Identify the blood parasite species.
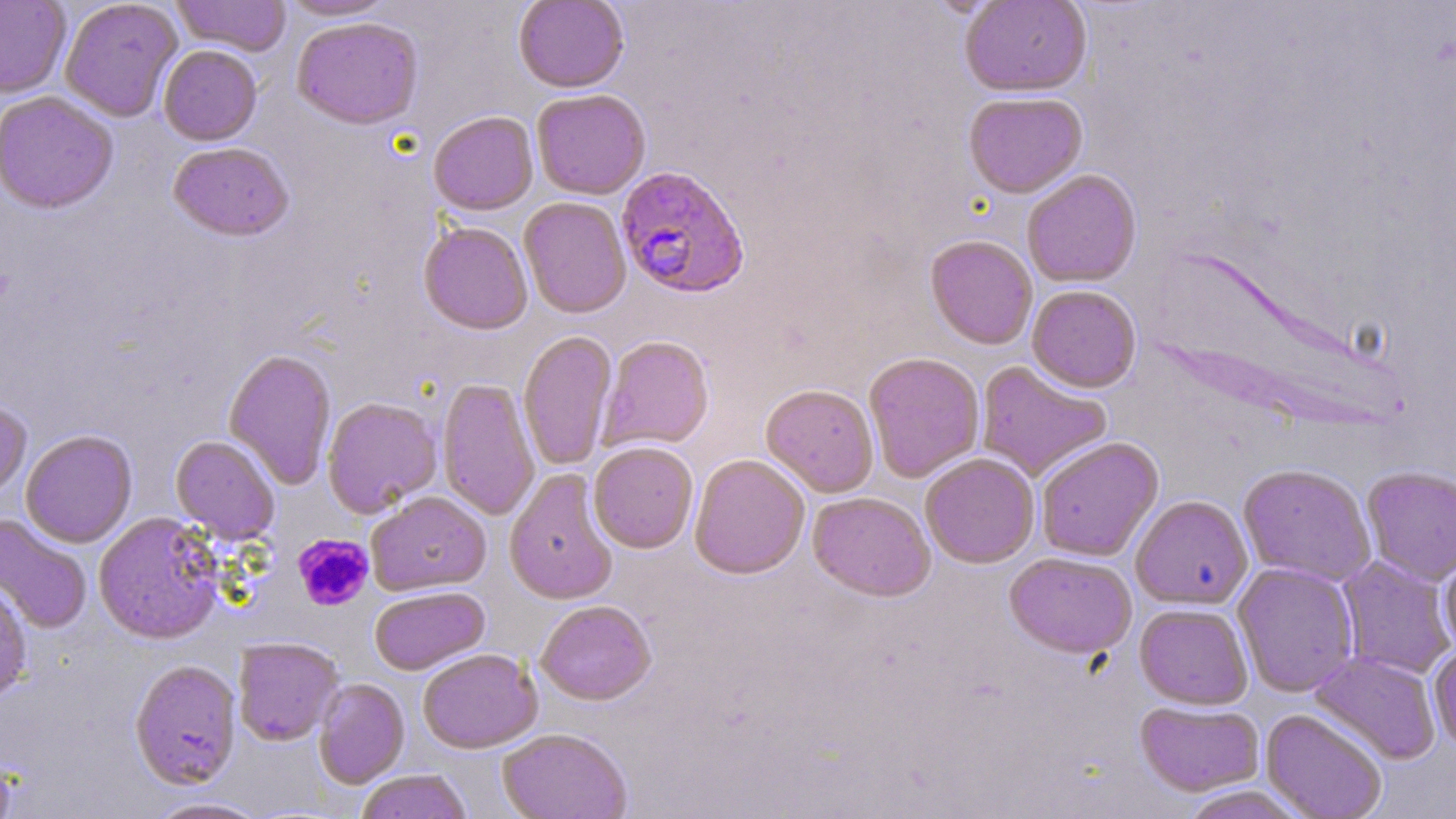

Plasmodium falciparum.

Summary:
  - Coordinate format: approximate bounding boxes as [x1, y1, x2, y2] in pixels
  - Uninfected red blood cell locations: [0, 0, 70, 99], [60, 0, 183, 122], [172, 0, 291, 56], [277, 0, 396, 21], [960, 0, 1092, 97], [514, 1, 629, 94], [291, 17, 424, 130], [158, 45, 262, 146], [532, 90, 651, 200], [1, 92, 118, 214], [963, 92, 1087, 198], [428, 112, 538, 216], [167, 142, 294, 242], [1022, 169, 1142, 288], [518, 197, 631, 319], [418, 221, 533, 335], [925, 235, 1038, 350], [1027, 285, 1142, 392], [518, 331, 618, 471], [598, 336, 714, 452], [224, 349, 337, 490], [863, 352, 985, 482], [975, 361, 1112, 482], [437, 378, 540, 521], [761, 383, 879, 498], [322, 397, 442, 517], [0, 402, 31, 502], [21, 430, 138, 548], [170, 435, 280, 543], [1036, 437, 1163, 561], [588, 441, 698, 554], [689, 453, 810, 579], [920, 453, 1040, 568], [1238, 463, 1377, 586], [1361, 466, 1456, 586], [504, 468, 618, 604], [366, 491, 491, 595], [807, 491, 935, 601], [1131, 494, 1253, 610], [93, 512, 224, 645], [0, 513, 92, 633], [1438, 544, 1456, 656], [1004, 552, 1137, 658], [1337, 556, 1455, 680], [1232, 562, 1359, 697], [0, 578, 33, 704], [369, 586, 489, 675], [536, 600, 656, 705], [1135, 603, 1253, 709], [233, 638, 343, 746], [1428, 640, 1456, 752], [417, 648, 542, 754], [1309, 651, 1442, 764], [130, 660, 241, 790], [313, 679, 409, 788], [1136, 700, 1265, 796], [1261, 708, 1388, 819], [497, 728, 632, 819], [355, 770, 473, 819], [1174, 785, 1313, 819], [143, 797, 271, 818]
  - Platelet locations: [293, 533, 374, 611]
  - Plasmodium falciparum-infected red blood cell locations: [615, 164, 751, 299]
  - Field of view: one of a larger specimen
  - Preparation: thin blood smear
  - Magnification: 1000x
  - Image size: 1456×819 pixels
  - Stain: May-Grünwald-Giemsa
  - Modality: light microscopy